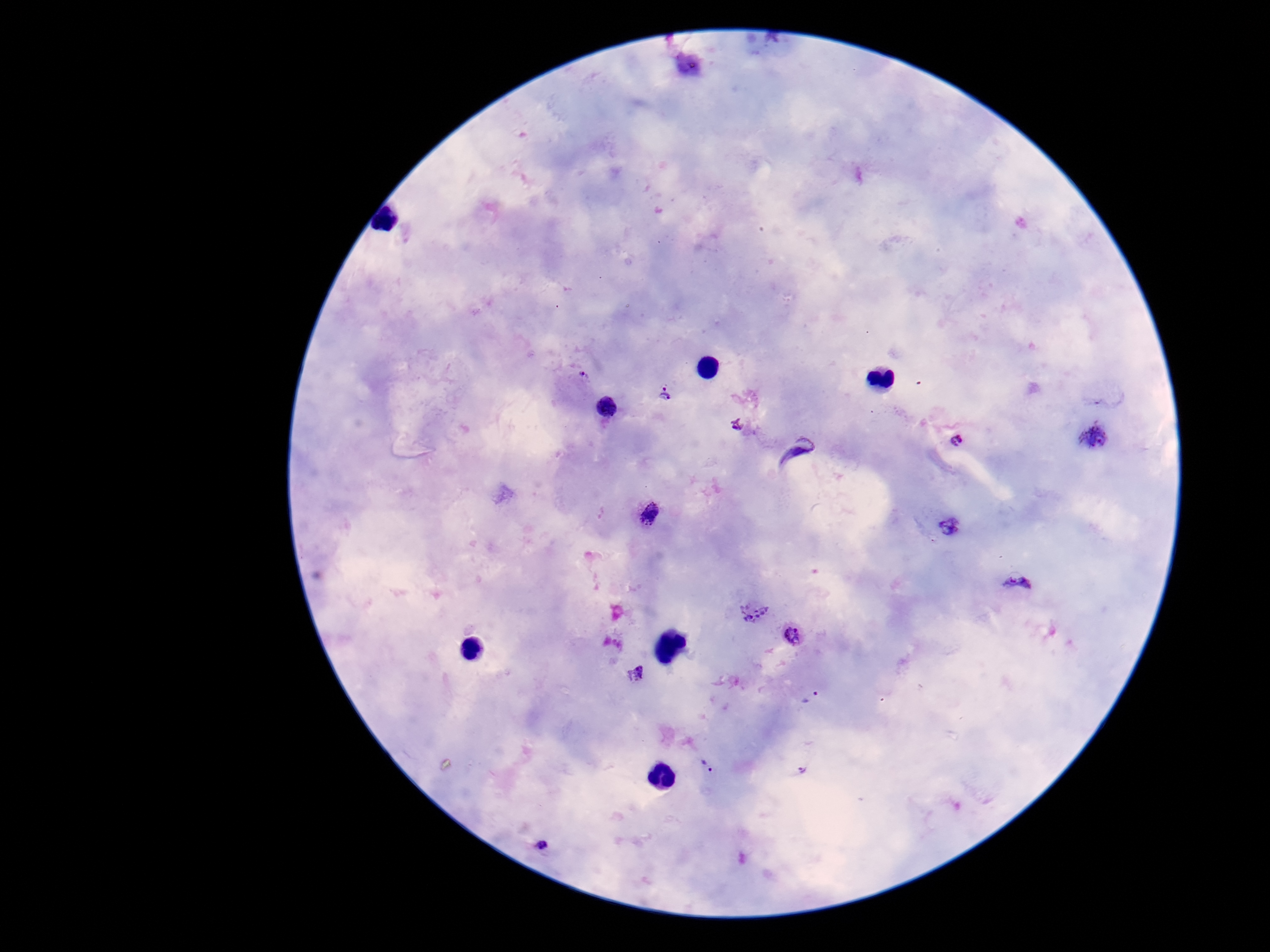
{
  "patient_malaria_status": "infected",
  "image_size": "1270×952 pixels",
  "field_of_view": "one from this slide",
  "capture": "smartphone camera through the microscope eyepiece",
  "magnification": "100x",
  "plasmodium_parasite_locations": "approximate object centers, in pixels from the top-left corner: (x=687, y=65), (x=581, y=377), (x=666, y=395), (x=737, y=423), (x=1093, y=436), (x=957, y=441), (x=796, y=450), (x=649, y=513), (x=950, y=529), (x=1020, y=585), (x=752, y=612), (x=794, y=635), (x=638, y=674), (x=813, y=698), (x=708, y=768), (x=804, y=770), (x=540, y=847)",
  "preparation": "thick peripheral-blood smear",
  "stain": "Giemsa"
}